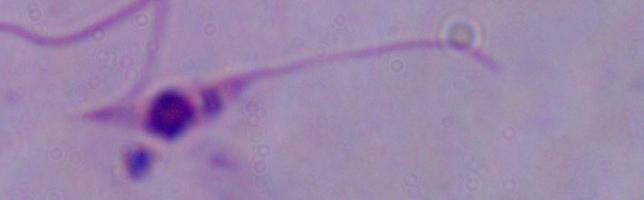

identification = Leishmania
modality = micrograph
magnification = 1000x